State which parasite is depicted.
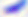

This is Toxoplasma gondii.

Micrograph. Captured at 400x magnification.